State the blood parasite species.
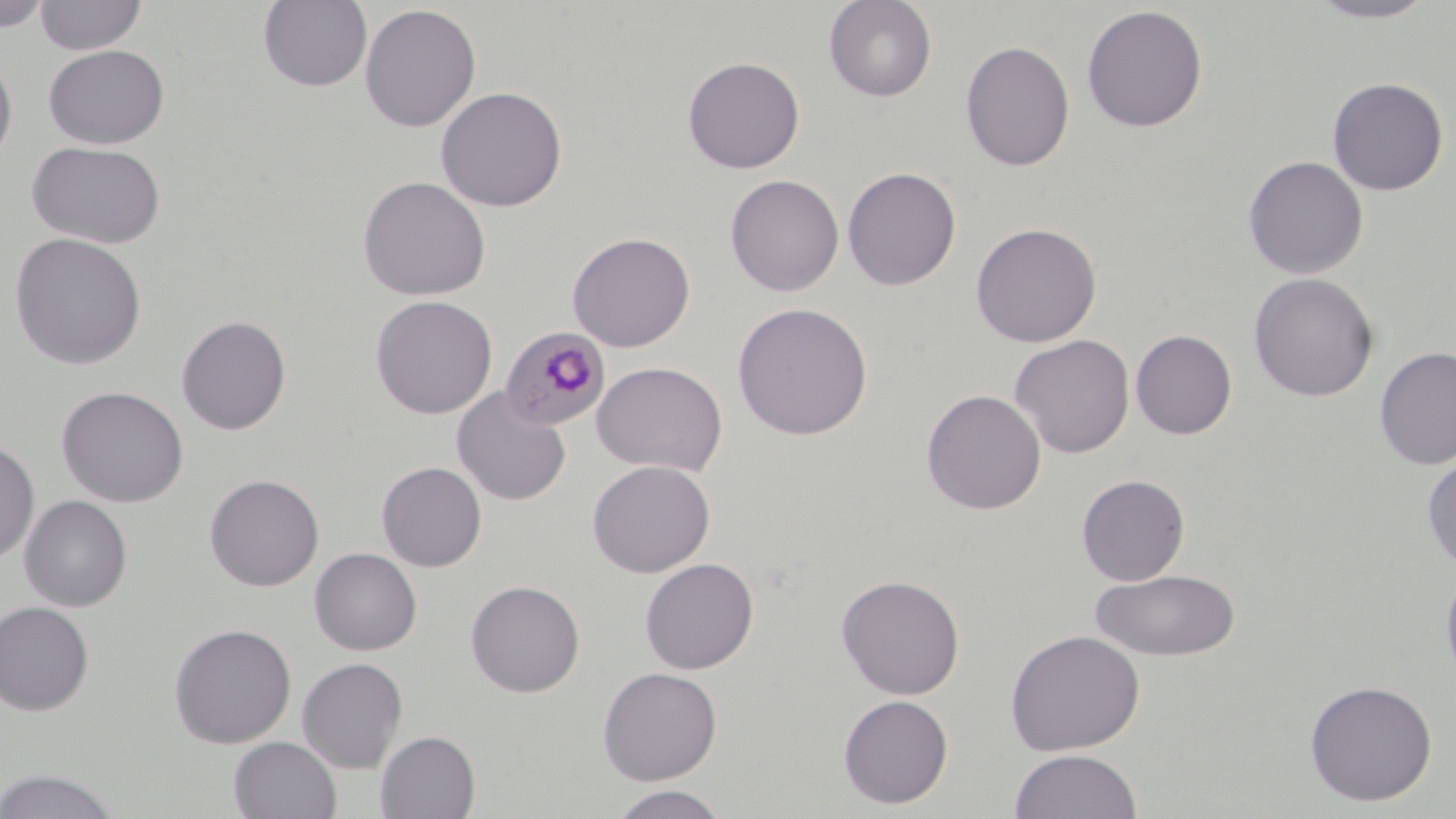

Plasmodium malariae.

Approximate bounding boxes as (x1,y1)-(x2,y2) corner pairs in pixels. Uninfected red blood cell locations: (0,0)-(51,32), (34,0)-(147,56), (823,0)-(937,102), (1306,0)-(1439,23), (258,1)-(373,92), (359,4)-(482,132), (1081,4)-(1208,132), (960,40)-(1075,171), (43,44)-(169,149), (0,54)-(18,168), (682,56)-(805,174), (1327,77)-(1448,196), (435,86)-(568,212), (26,140)-(167,250), (1243,155)-(1369,279), (842,167)-(961,290), (724,174)-(845,297), (357,175)-(491,301), (970,222)-(1102,347), (8,232)-(147,371), (567,232)-(695,352), (1248,272)-(1379,402), (370,295)-(497,418), (732,302)-(873,440), (176,315)-(291,435), (1130,329)-(1237,439), (1010,334)-(1135,458), (1374,346)-(1456,471), (591,361)-(728,477), (56,386)-(189,508), (452,387)-(571,506), (921,388)-(1046,515), (0,439)-(40,564), (1422,451)-(1456,571), (586,459)-(715,577), (376,461)-(487,572), (204,474)-(324,591), (1076,474)-(1190,586), (19,494)-(132,611), (309,547)-(422,655), (640,557)-(759,673), (1439,563)-(1456,693), (1090,568)-(1241,661), (836,573)-(965,700), (465,580)-(585,698), (0,601)-(95,716), (168,623)-(297,748), (1004,629)-(1146,756), (296,657)-(408,773), (597,666)-(722,785), (1303,679)-(1438,806), (837,694)-(954,809), (375,730)-(480,818), (228,736)-(342,819), (1008,749)-(1143,819), (0,767)-(125,819), (606,785)-(732,819). Plasmodium malariae-infected red blood cell locations: (501,326)-(610,431). Optical microscopy. 1000x magnification. May-Grünwald-Giemsa stain. Thin blood smear. One field of a larger specimen. Image is 1456×819 pixels.